Report the malaria status of this cell.
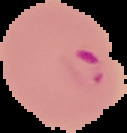

Parasitized.

image size = 127×133 pixels
image type = cell region segmented out of the field of view; surrounding area masked to black
preparation = thin blood smear